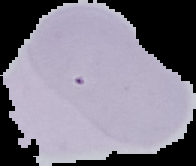
result = no Plasmodium parasites seen
preparation = thin blood film
image type = segmented cell region with the area outside set to black
image size = 196×166 pixels